Identify the cell.
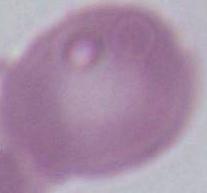
An erythrocyte.

Summary:
  - Magnification: 1000x
  - Modality: photomicrograph